Name the parasite shown.
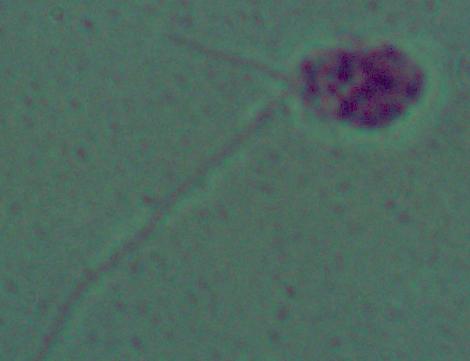

This is Leishmania.

Micrograph. 1000x magnification.